Report the malaria status of this cell.
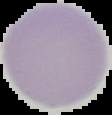
It is uninfected.

image type = segmented cell region on a black background
preparation = thin blood smear
image size = 112×115 pixels